Report the malaria status of this cell.
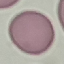
Uninfected.

stain = Giemsa
capture = smartphone through the microscope eyepiece
image type = automatically extracted cell patch, resized to 64 × 64 pixels
preparation = thin smear